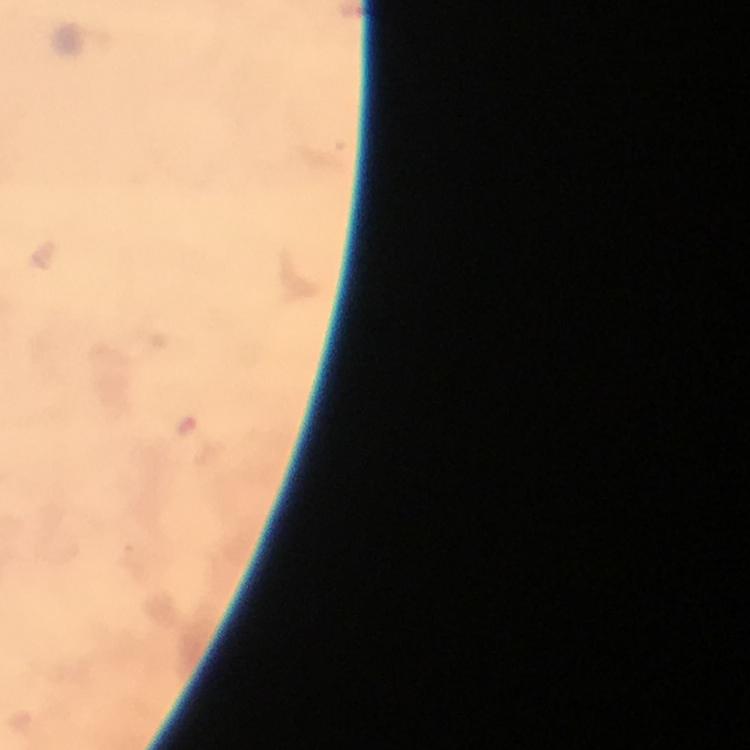

context = from a malaria diagnostic workup
cropped from = one field of view
preparation = thick smear
stain = Giemsa
immersion oil = used
capture = smartphone mounted on the microscope
magnification = 100x
image size = 750×750 pixels
Plasmodium parasite locations = approximate object centers, in pixels from the top-left corner: (x=187, y=424)